Identify the preparation type.
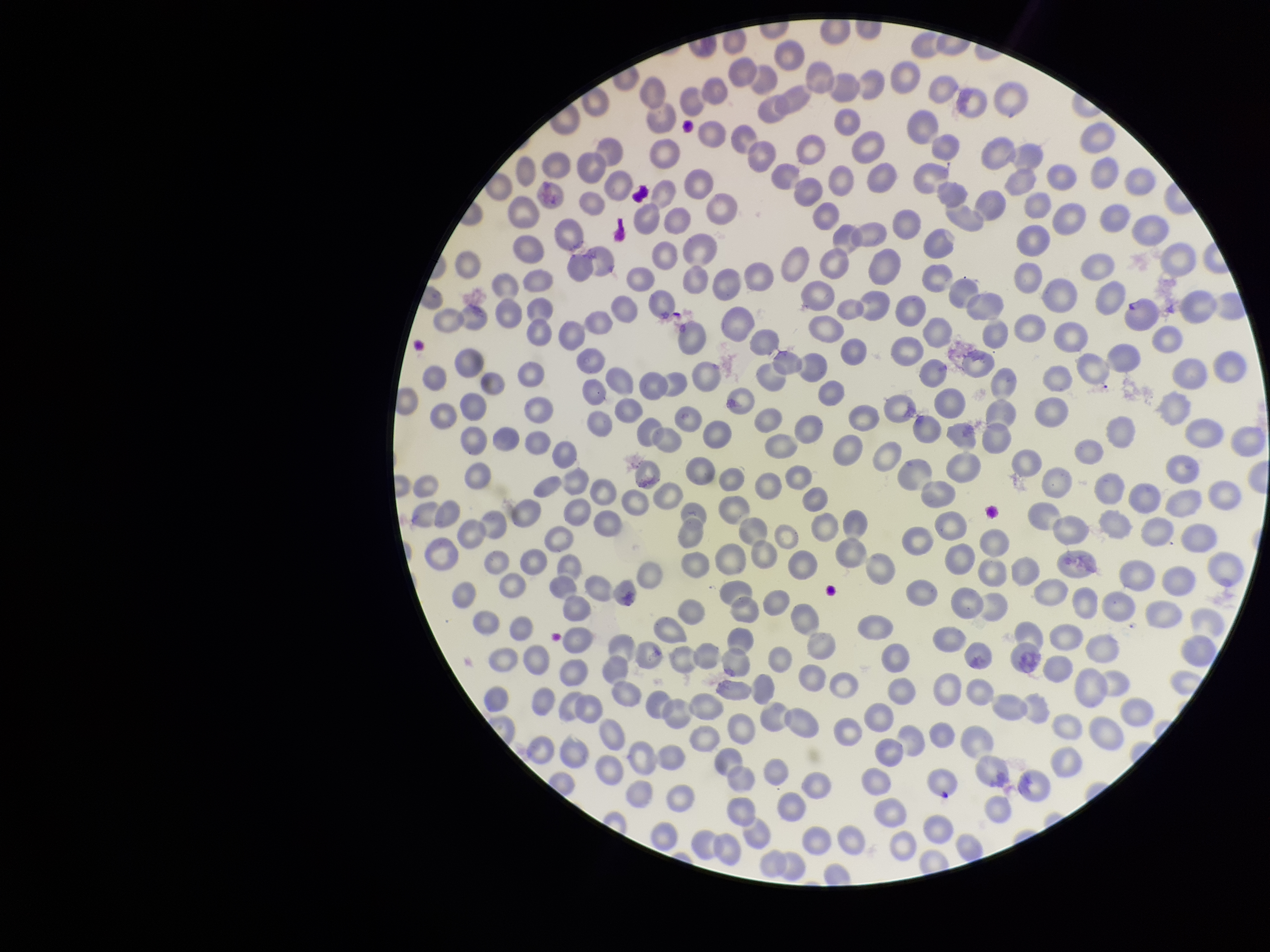

It is a thin blood smear.

Single field of view. Parasitized red blood cell count: 0. Smartphone photograph taken through the eyepiece of a microscope. Parasitized red blood cells: none identified. Giemsa stain. Red blood cell count: 333. Species reported for this patient: Plasmodium falciparum. Patient malaria status: infected. Image is 1270×952 pixels.